Assess this cell for malaria.
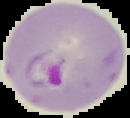

Parasitized.

image size = 130×118 pixels
image type = segmented cell region on a black background
preparation = thin blood film